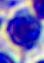
modality: micrograph
identification: leukocyte
magnification: 400x